Locate every blood parasite and identify its species.
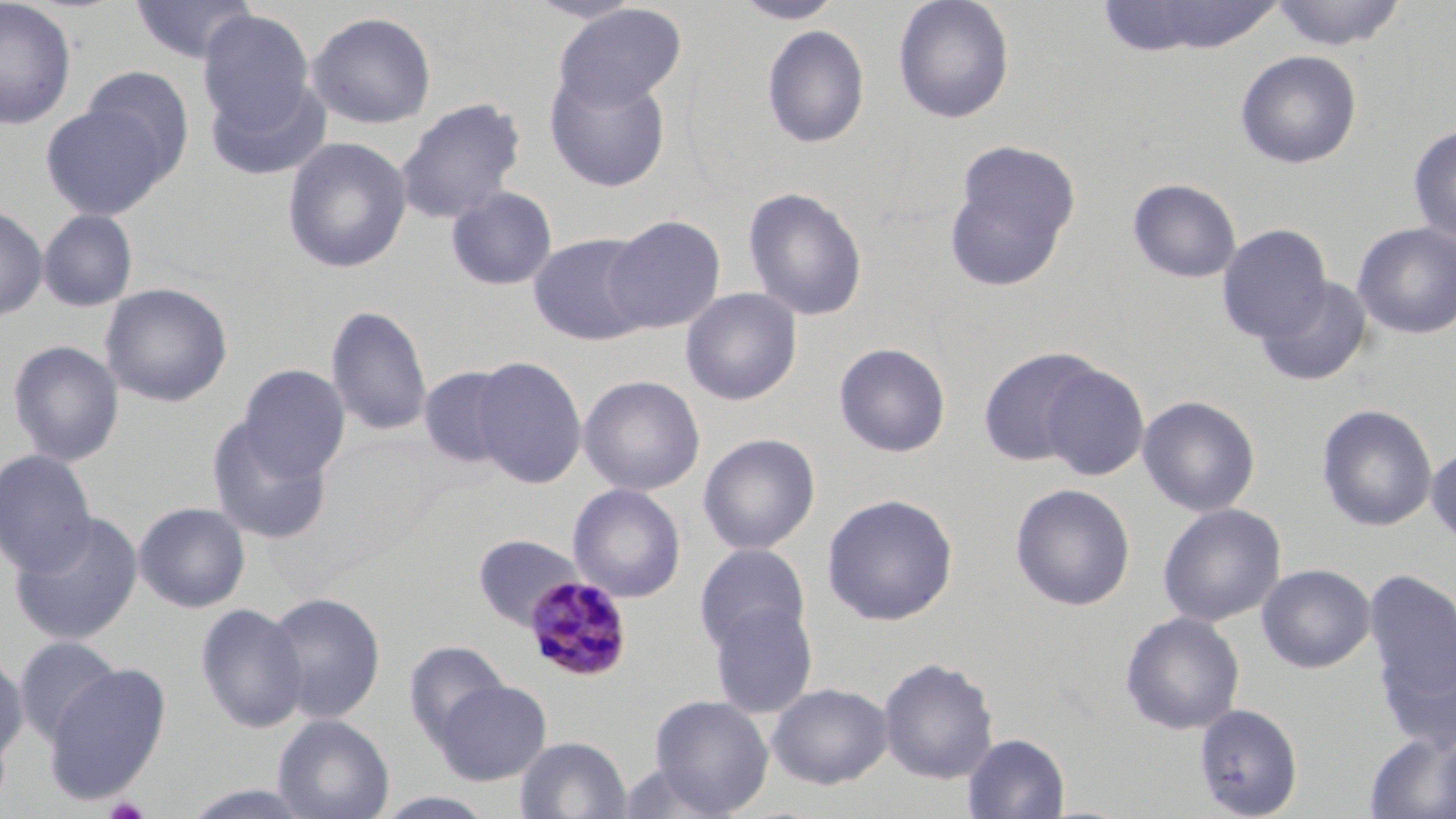
Approximate bounding boxes as named x1/y1/x2/y2 corners in pixels.
Plasmodium malariae-infected red blood cells: (x1=523, y1=576, x2=633, y2=683).
No Plasmodium falciparum, Plasmodium ovale, Plasmodium vivax, Babesia divergens, or Trypanosoma brucei observed.

Uninfected red blood cell locations: (x1=0, y1=0, x2=77, y2=130), (x1=130, y1=0, x2=257, y2=64), (x1=733, y1=0, x2=844, y2=24), (x1=893, y1=0, x2=1015, y2=124), (x1=1104, y1=0, x2=1287, y2=56), (x1=1270, y1=1, x2=1408, y2=51), (x1=554, y1=3, x2=685, y2=111), (x1=197, y1=10, x2=316, y2=134), (x1=307, y1=11, x2=437, y2=129), (x1=762, y1=25, x2=870, y2=148), (x1=1235, y1=50, x2=1362, y2=169), (x1=81, y1=66, x2=195, y2=178), (x1=545, y1=69, x2=671, y2=192), (x1=206, y1=75, x2=331, y2=182), (x1=395, y1=97, x2=525, y2=225), (x1=40, y1=103, x2=171, y2=219), (x1=1408, y1=123, x2=1456, y2=245), (x1=282, y1=137, x2=412, y2=274), (x1=943, y1=139, x2=1081, y2=291), (x1=1127, y1=178, x2=1242, y2=283), (x1=446, y1=186, x2=558, y2=291), (x1=743, y1=186, x2=868, y2=321), (x1=0, y1=205, x2=48, y2=322), (x1=38, y1=209, x2=138, y2=312), (x1=603, y1=215, x2=727, y2=334), (x1=1352, y1=222, x2=1456, y2=339), (x1=1216, y1=224, x2=1331, y2=343), (x1=527, y1=232, x2=654, y2=346), (x1=1256, y1=277, x2=1373, y2=388), (x1=99, y1=282, x2=233, y2=408), (x1=680, y1=287, x2=802, y2=406), (x1=325, y1=304, x2=433, y2=437), (x1=7, y1=340, x2=125, y2=467), (x1=833, y1=342, x2=951, y2=458), (x1=977, y1=346, x2=1106, y2=467), (x1=472, y1=356, x2=587, y2=489), (x1=238, y1=363, x2=350, y2=479), (x1=1038, y1=363, x2=1150, y2=480), (x1=418, y1=366, x2=518, y2=469), (x1=578, y1=375, x2=705, y2=496), (x1=1138, y1=395, x2=1261, y2=517), (x1=1316, y1=404, x2=1437, y2=532), (x1=206, y1=415, x2=332, y2=544), (x1=698, y1=433, x2=820, y2=555), (x1=1426, y1=442, x2=1456, y2=551), (x1=0, y1=449, x2=97, y2=576), (x1=568, y1=483, x2=686, y2=603), (x1=1010, y1=483, x2=1135, y2=611), (x1=821, y1=493, x2=959, y2=626), (x1=134, y1=502, x2=251, y2=613), (x1=1157, y1=503, x2=1286, y2=627), (x1=10, y1=511, x2=144, y2=645), (x1=473, y1=534, x2=585, y2=630), (x1=694, y1=543, x2=811, y2=655), (x1=1257, y1=563, x2=1375, y2=673), (x1=1365, y1=569, x2=1456, y2=700), (x1=263, y1=591, x2=386, y2=724), (x1=706, y1=600, x2=818, y2=718), (x1=195, y1=602, x2=307, y2=733), (x1=1120, y1=611, x2=1245, y2=735), (x1=1375, y1=627, x2=1456, y2=757), (x1=14, y1=635, x2=123, y2=745), (x1=404, y1=640, x2=510, y2=748), (x1=0, y1=651, x2=28, y2=765), (x1=878, y1=657, x2=999, y2=784), (x1=43, y1=663, x2=171, y2=804), (x1=435, y1=679, x2=551, y2=785), (x1=767, y1=682, x2=893, y2=789), (x1=649, y1=695, x2=774, y2=816), (x1=1194, y1=702, x2=1304, y2=818), (x1=273, y1=714, x2=394, y2=819), (x1=1364, y1=729, x2=1456, y2=819), (x1=962, y1=733, x2=1070, y2=819), (x1=515, y1=736, x2=632, y2=818), (x1=615, y1=761, x2=733, y2=819). Slide-level diagnosis: Plasmodium malariae. Optical microscopy. One field of a larger specimen. Image is 1456×819 pixels. May-Grünwald-Giemsa-stained preparation. Thin blood smear. Captured at 1000x magnification.